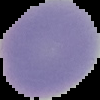

image type = segmented cell region on a black background
malaria status = uninfected
image size = 100×100 pixels
preparation = thin blood smear